State which parasite is depicted.
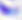

Toxoplasma gondii.

magnification = 400x
modality = micrograph